Locate and identify every blood parasite.
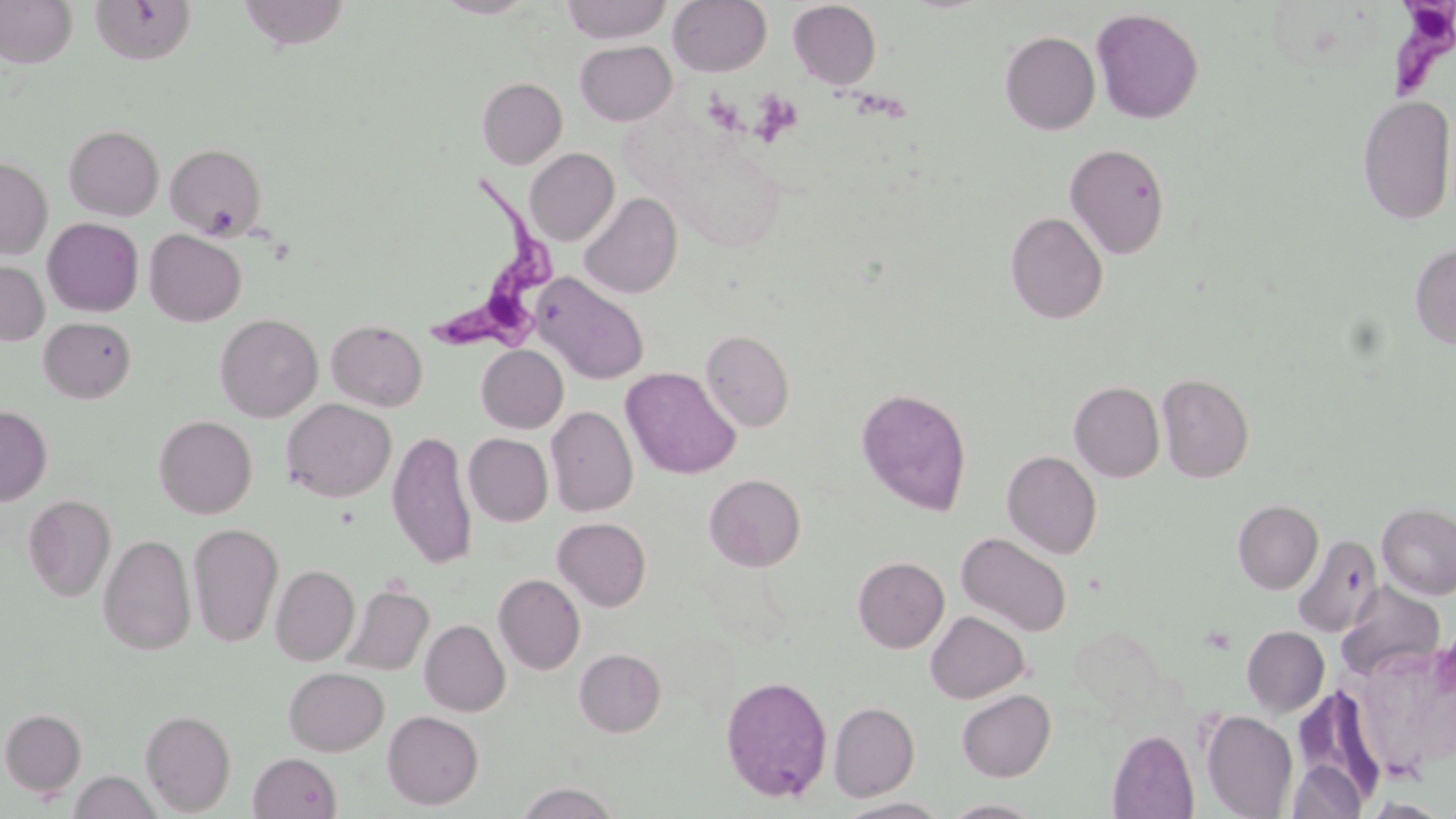
Approximate bounding boxes as (x1,y1)-(x2,y2) corner pairs in pixels.
Trypanosoma brucei: (1382,3)-(1455,103), (424,174)-(566,357).
No Plasmodium falciparum, Plasmodium ovale, Plasmodium malariae, Plasmodium vivax, or Babesia divergens observed.

Uninfected red blood cell locations: (0,0)-(78,68), (237,0)-(352,50), (435,0)-(537,18), (562,0)-(671,43), (668,0)-(771,76), (91,1)-(197,65), (788,1)-(882,89), (1091,8)-(1204,125), (1000,30)-(1100,134), (575,40)-(676,125), (477,77)-(567,169), (1358,95)-(1455,225), (64,125)-(164,220), (165,143)-(266,239), (1064,143)-(1170,259), (525,148)-(619,245), (0,157)-(52,259), (579,192)-(682,299), (1005,212)-(1108,324), (43,218)-(144,317), (145,230)-(246,326), (1410,243)-(1456,350), (0,261)-(49,346), (533,273)-(649,384), (215,313)-(323,422), (39,317)-(136,403), (326,319)-(428,411), (700,329)-(794,432), (476,345)-(568,433), (621,366)-(741,480), (1157,373)-(1254,483), (1069,381)-(1165,482), (857,387)-(972,515), (281,398)-(396,502), (0,405)-(52,506), (546,406)-(637,516), (154,415)-(257,519), (387,430)-(477,570), (464,433)-(553,526), (1002,450)-(1102,558), (704,474)-(805,571), (23,495)-(116,602), (1233,499)-(1323,593), (1377,502)-(1456,599), (553,517)-(651,611), (188,523)-(283,647), (956,532)-(1072,637), (99,535)-(196,655), (1293,535)-(1383,637), (853,556)-(949,652), (271,565)-(359,666), (493,574)-(585,674), (1336,582)-(1445,683), (342,583)-(434,676), (925,611)-(1029,703), (420,619)-(510,716), (1242,626)-(1329,717), (575,648)-(666,737), (284,666)-(389,755), (720,675)-(833,803), (956,689)-(1055,782), (829,702)-(919,800), (1,708)-(86,797), (140,709)-(236,815), (383,710)-(483,809), (1201,710)-(1298,818), (1108,730)-(1199,818), (248,753)-(341,818), (1287,759)-(1365,819), (69,770)-(160,818), (515,782)-(621,819), (836,796)-(950,819), (943,798)-(1046,818). Slide-level diagnosis: Trypanosoma brucei. Optical microscopy. Thin blood film. 1000x magnification. Image is 1456×819 pixels. Single field of view. May-Grünwald-Giemsa stain.